Report the malaria status of this cell.
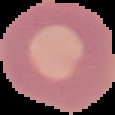
It is uninfected.

Summary:
  - Image size: 115×115 pixels
  - Image type: cell region segmented out of the field of view; surrounding area masked to black
  - Preparation: thin blood film